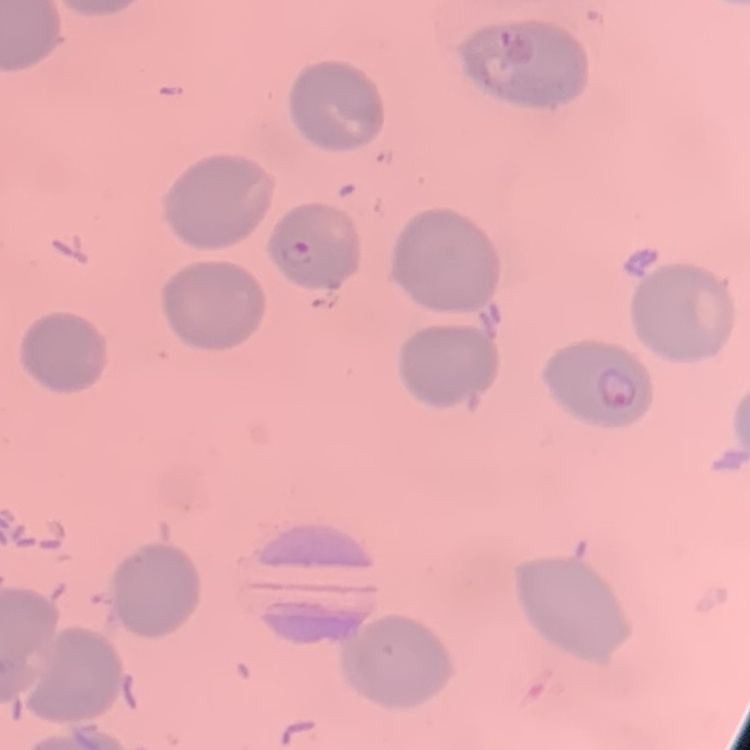

erythrocyte morphology = no rouleaux formation
preparation = thin peripheral smear
image type = square crop of a larger photomicrograph
stain = Field's or Giemsa